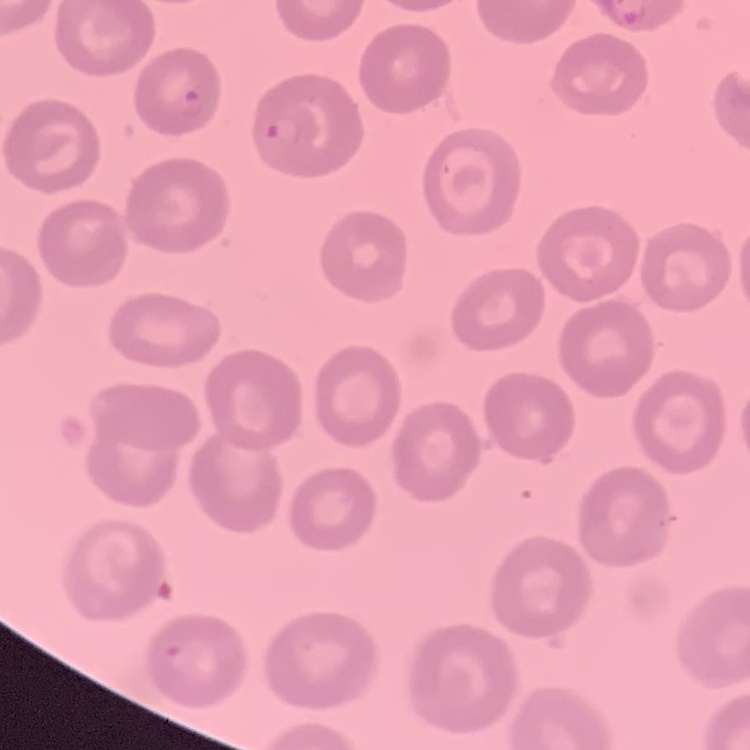
red blood cell morphology = no rouleaux formation
stain = Field's or Giemsa
image type = one tile cut from a larger photomicrograph
preparation = thin blood smear